Name the blood parasite species.
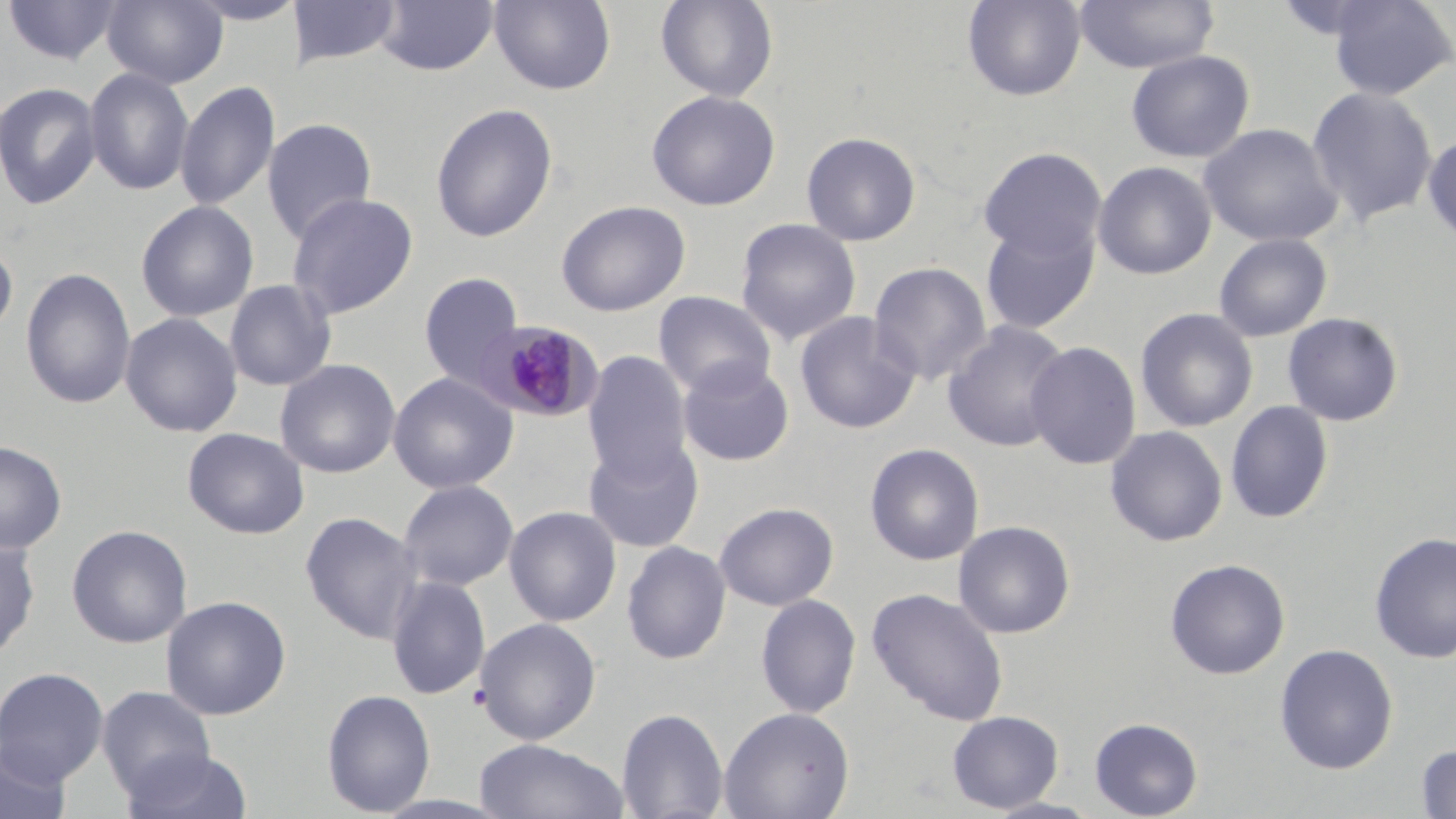
Plasmodium malariae.

Approximate bounding boxes as (x1,y1)-(x2,y2) corner pairs in pixels. Plasmodium malariae-infected red blood cell locations: (475,320)-(604,423). Uninfected red blood cell locations: (102,0)-(228,89), (184,0)-(304,26), (294,0)-(400,69), (375,0)-(499,77), (489,0)-(616,94), (655,0)-(779,102), (962,0)-(1087,101), (1075,0)-(1218,73), (1326,0)-(1456,101), (3,1)-(124,65), (1126,49)-(1255,163), (84,67)-(195,196), (175,80)-(280,213), (0,81)-(102,210), (1307,86)-(1438,227), (646,89)-(780,211), (430,103)-(558,242), (262,117)-(378,244), (1199,123)-(1343,247), (801,131)-(921,246), (1422,132)-(1456,249), (978,147)-(1106,259), (1093,161)-(1217,280), (286,192)-(418,319), (135,200)-(259,322), (555,200)-(690,317), (735,218)-(861,345), (979,218)-(1099,335), (1213,232)-(1333,342), (0,238)-(18,341), (868,261)-(992,386), (21,266)-(136,410), (418,272)-(525,391), (224,279)-(337,391), (652,291)-(776,399), (1135,308)-(1258,432), (794,311)-(921,434), (120,312)-(242,438), (1282,312)-(1404,427), (943,320)-(1072,453), (1025,341)-(1142,470), (582,351)-(692,485), (274,358)-(401,479), (677,358)-(795,467), (387,372)-(518,494), (1225,401)-(1334,524), (1105,425)-(1228,547), (182,427)-(309,539), (584,438)-(702,553), (0,440)-(66,553), (864,442)-(985,566), (398,479)-(519,591), (714,501)-(839,611), (504,506)-(621,626), (300,510)-(423,644), (953,520)-(1076,638), (66,524)-(193,648), (1370,531)-(1456,663), (0,536)-(40,662), (621,540)-(731,665), (1164,558)-(1290,680), (385,576)-(490,699), (867,586)-(1009,726), (756,593)-(861,719), (160,595)-(291,720), (476,617)-(602,745), (1274,643)-(1398,774), (0,666)-(109,785), (96,684)-(216,802), (321,688)-(436,816), (616,707)-(729,819), (718,707)-(854,819), (947,710)-(1064,812), (1089,717)-(1203,819), (473,737)-(629,819), (1,742)-(72,819), (1415,744)-(1456,818), (120,748)-(254,819), (983,797)-(1104,819). Thin blood film. 1000x magnification. Single field of view. Optical microscopy. Image is 1456×819 pixels. May-Grünwald-Giemsa-stained preparation.